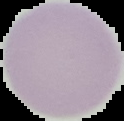

The area outside the segmented cell region is set to black. Image is 124×121 pixels. Malaria status: uninfected. From a thin blood film.